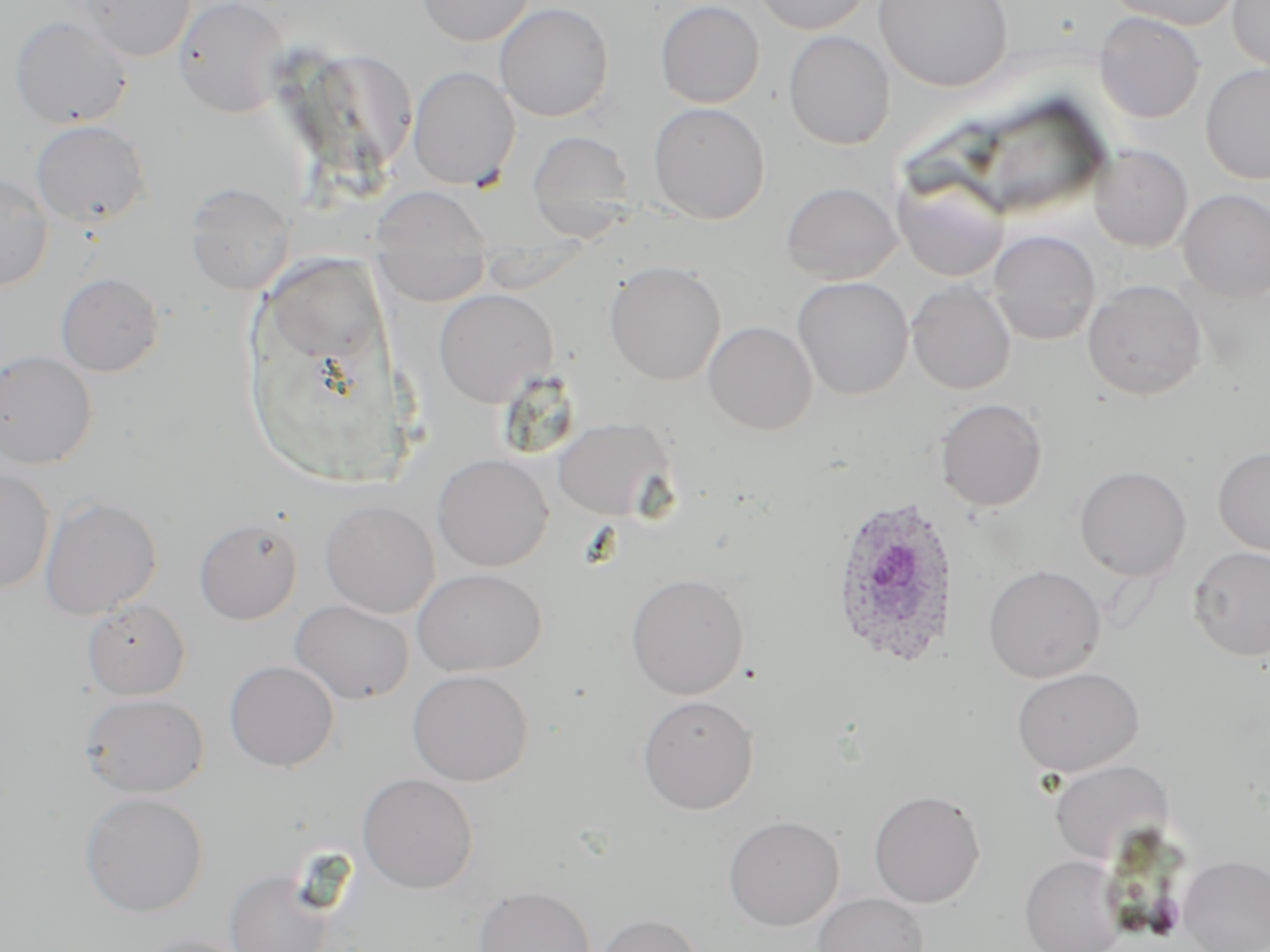
Summary:
  - Coordinate format: approximate bounding boxes as [x1, y1, x2, y2] in pixels
  - Plasmodium ovale-infected red blood cell locations: [828, 493, 962, 669]
  - Uninfected red blood cell locations: [77, 0, 196, 61], [173, 0, 289, 117], [416, 0, 533, 46], [655, 0, 765, 108], [750, 0, 873, 35], [875, 0, 1012, 91], [1108, 0, 1242, 30], [1228, 0, 1270, 73], [494, 2, 614, 121], [1094, 11, 1206, 123], [10, 16, 134, 129], [783, 31, 895, 150], [1200, 64, 1270, 184], [407, 66, 520, 190], [648, 102, 770, 224], [31, 120, 151, 227], [527, 130, 636, 237], [1089, 144, 1193, 252], [892, 171, 1010, 282], [0, 173, 53, 291], [780, 181, 901, 284], [185, 182, 296, 295], [373, 187, 488, 256], [1178, 189, 1270, 302], [985, 230, 1102, 346], [375, 254, 489, 306], [604, 261, 726, 386], [56, 272, 165, 377], [792, 276, 914, 400], [1082, 279, 1207, 400], [907, 280, 1016, 395], [433, 288, 557, 407], [703, 320, 818, 434], [0, 349, 97, 468], [935, 398, 1048, 512], [552, 417, 675, 521], [1213, 446, 1270, 557], [432, 454, 554, 572], [1074, 465, 1192, 580], [0, 468, 55, 593], [39, 495, 162, 620], [320, 500, 440, 618], [194, 517, 302, 625], [1188, 545, 1270, 661], [983, 564, 1106, 683], [412, 568, 546, 676], [626, 572, 749, 699], [82, 599, 190, 701], [289, 599, 415, 705], [224, 660, 340, 771], [1011, 666, 1144, 776], [407, 669, 534, 785], [80, 692, 210, 798], [637, 694, 759, 814], [1048, 759, 1174, 865], [356, 773, 478, 894], [868, 789, 986, 908], [79, 791, 209, 917], [723, 815, 844, 930], [1020, 854, 1125, 952], [1178, 855, 1270, 952], [225, 869, 334, 952], [474, 885, 597, 952], [812, 892, 930, 952], [591, 912, 704, 952], [132, 934, 253, 952]
  - Slide-level diagnosis: Plasmodium ovale
  - Preparation: thin blood film
  - Field of view: one of a larger specimen
  - Modality: optical microscopy
  - Stain: May-Grünwald-Giemsa
  - Image size: 1270×952 pixels
  - Magnification: 1000x